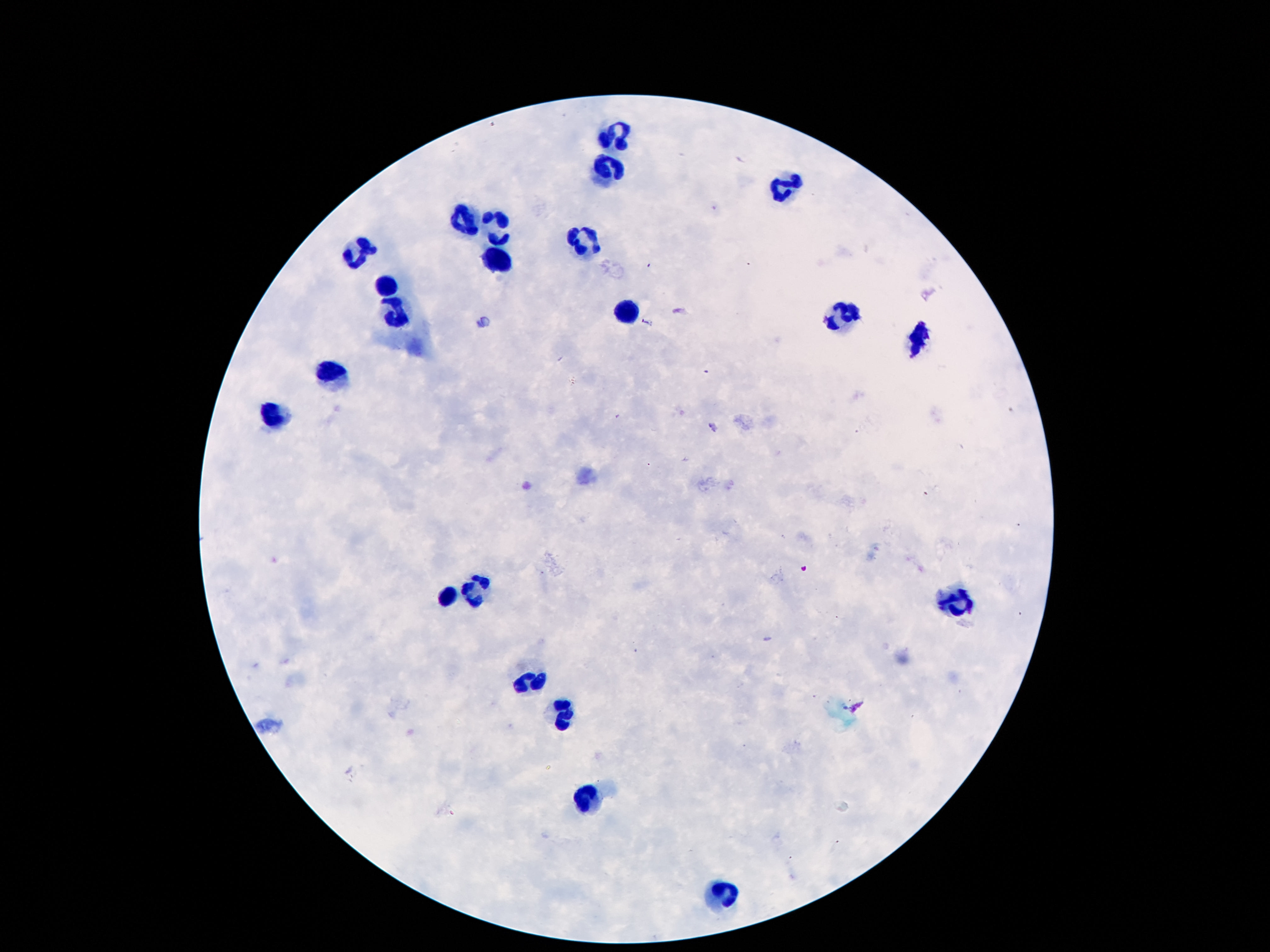
Approximate object centers, in pixels from the top-left corner.
Summary:
  - Leukocyte locations: (x=612, y=135), (x=609, y=168), (x=784, y=184), (x=495, y=217), (x=467, y=220), (x=586, y=240), (x=359, y=252), (x=499, y=260), (x=385, y=286), (x=631, y=311), (x=848, y=315), (x=400, y=316), (x=922, y=339), (x=332, y=370), (x=276, y=416), (x=476, y=591), (x=451, y=594), (x=957, y=602), (x=528, y=685), (x=566, y=713), (x=591, y=795), (x=725, y=895)
  - Stain: Giemsa
  - Capture: smartphone camera through the microscope eyepiece
  - Magnification: 100x
  - Patient malaria status: uninfected
  - Preparation: thick blood smear
  - Field of view: one from this slide
  - Image size: 1270×952 pixels